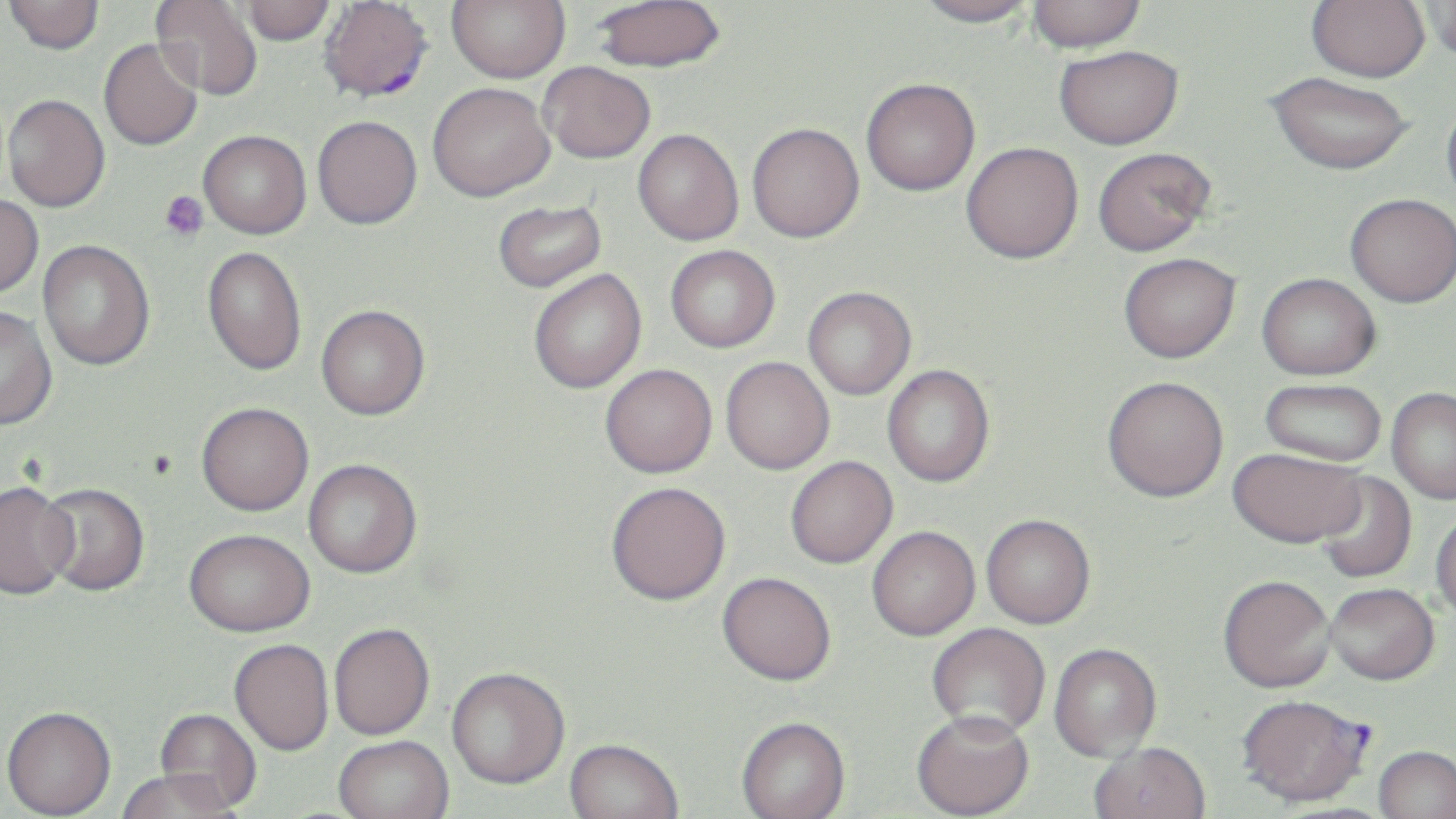
slide_level_diagnosis: Plasmodium falciparum
platelet_locations: 'approximate bounding boxes as (x1, y1, x2, y2) in pixels: (160, 190, 209, 242)'
field_of_view: single
preparation: thin blood smear
image_size: 1456×819 pixels
stain: May-Grünwald-Giemsa
modality: optical microscopy
magnification: 1000x
uninfected_red_blood_cell_locations_subset: 'approximate bounding boxes as (x1, y1, x2, y2) in pixels: (3, 0, 105, 54), (150, 0, 264, 101), (447, 0, 569, 83), (592, 0, 726, 72), (913, 0, 1038, 28), (1027, 0, 1146, 53), (1306, 0, 1430, 82), (240, 1, 337, 45), (1423, 1, 1456, 63), (99, 38, 203, 151), (1054, 44, 1184, 149), (539, 61, 656, 163), (1265, 71, 1415, 175), (861, 78, 980, 196), (427, 82, 555, 201), (2, 94, 110, 212), (1442, 97, 1456, 210), (313, 115, 422, 229), (747, 122, 864, 242), (633, 129, 743, 245), (198, 130, 311, 238), (961, 142, 1083, 263), (1092, 147, 1215, 256), (1345, 193, 1456, 307), (0, 195, 44, 298), (493, 199, 606, 292), (38, 240, 155, 371), (666, 245, 780, 352), (203, 246, 307, 377), (1118, 252, 1240, 363), (529, 269, 646, 393), (1257, 272, 1381, 380), (803, 286, 916, 399), (316, 304, 430, 420), (0, 306, 58, 431), (721, 356, 834, 475), (600, 364, 717, 478), (882, 365, 995, 487), (1102, 376, 1228, 502), (1259, 378, 1387, 467), (1386, 387, 1456, 504), (196, 402, 314, 515), (1228, 447, 1366, 548), (785, 456, 898, 568), (304, 458, 423, 578), (1313, 470, 1418, 585), (0, 481, 79, 600), (605, 481, 731, 604), (38, 482, 150, 596), (1430, 509, 1456, 625), (981, 514, 1095, 629), (867, 526, 980, 640), (182, 528, 315, 637), (717, 571, 836, 685), (1218, 575, 1335, 693), (1325, 583, 1439, 684), (927, 622, 1050, 739), (329, 623, 435, 741), (229, 639, 334, 757), (1049, 643, 1162, 761), (447, 667, 569, 790), (1, 708, 117, 819), (155, 708, 262, 812), (912, 710, 1034, 819), (736, 717, 851, 819), (333, 737, 455, 819), (564, 739, 683, 819), (1089, 742, 1212, 819), (1374, 746, 1456, 819), (117, 771, 241, 819)'